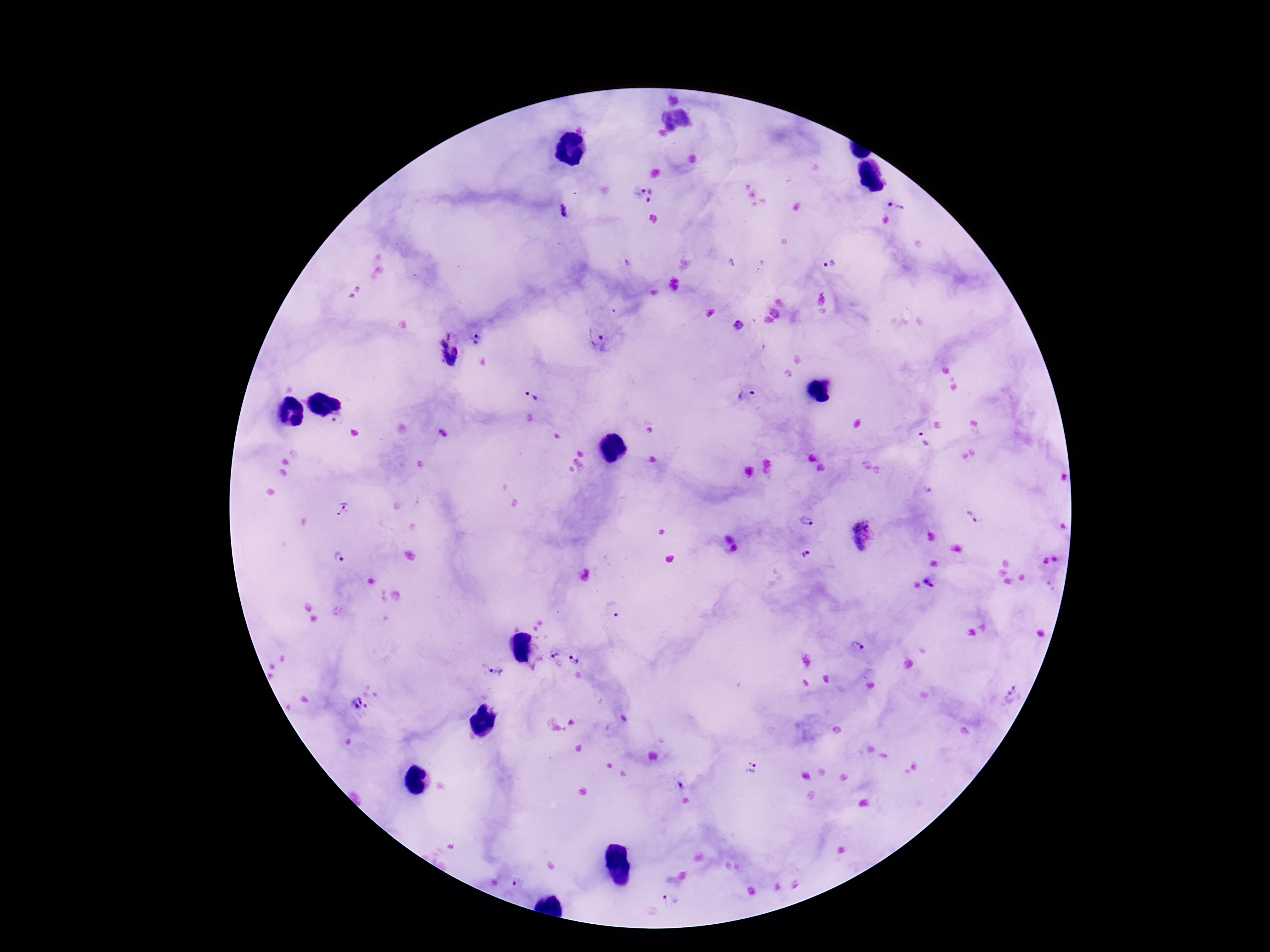
preparation = thick blood film
capture = smartphone camera through the microscope eyepiece
patient malaria status = positive
stain = Giemsa
image size = 1270×952 pixels
Plasmodium parasite locations = approximate centers as [x, y] in pixels: [644, 195], [895, 205], [564, 211], [828, 264], [738, 325], [478, 338], [598, 344], [448, 352], [531, 395], [747, 395], [338, 418], [923, 439], [344, 508], [972, 517], [806, 521], [861, 535], [733, 548], [805, 554], [340, 558], [930, 581], [613, 609], [857, 645], [555, 654], [574, 660], [495, 670], [1013, 693], [360, 706], [751, 769], [680, 784], [520, 884], [671, 900]
field of view = one from this slide
magnification = 100x